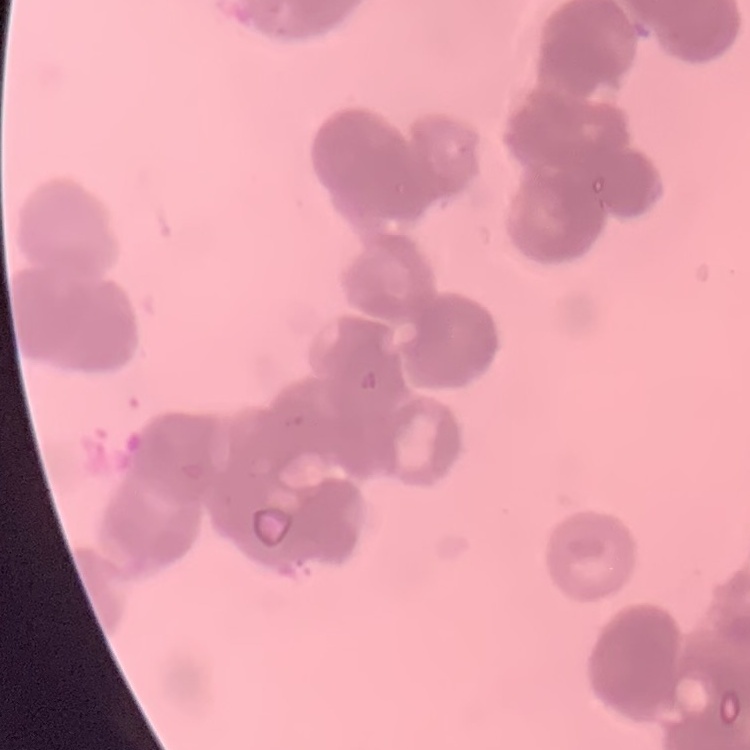
erythrocyte morphology = rouleaux formation
image type = square crop of a larger photomicrograph
preparation = thin peripheral smear
stain = Field's or Giemsa